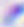
Summary:
  - Modality: photomicrograph
  - Magnification: 400x
  - Identification: Toxoplasma gondii